Locate every Plasmodium falciparum-infected red blood cell.
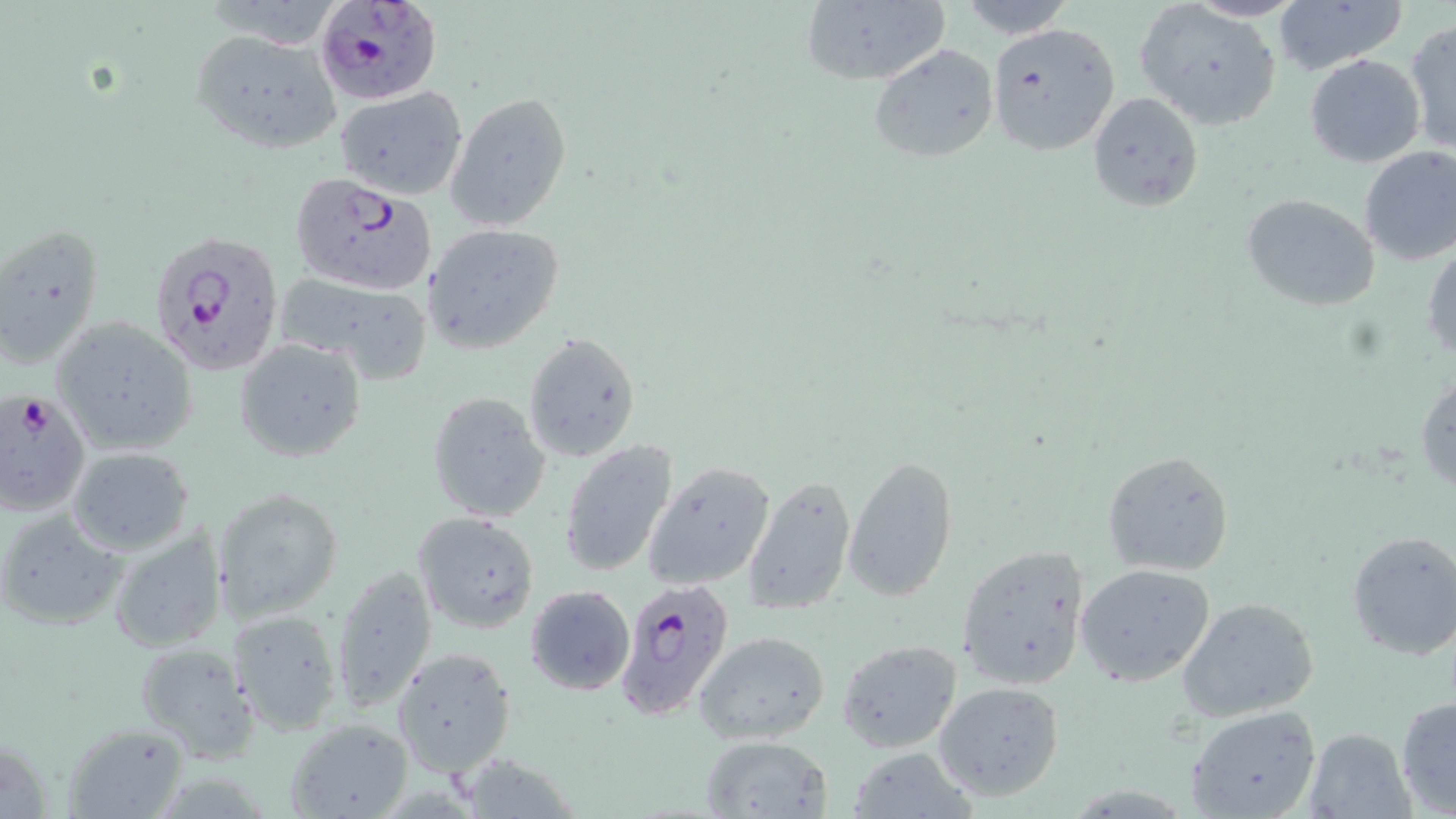
Approximate bounding boxes as (x1, y1, x2, y2) in pixels.
Plasmodium falciparum-infected red blood cells: (317, 0, 439, 103), (288, 171, 437, 295), (148, 229, 284, 376), (0, 391, 91, 516), (614, 580, 736, 722).

Summary:
  - Uninfected red blood cell locations: (798, 0, 948, 87), (1271, 0, 1408, 77), (955, 1, 1078, 39), (1137, 3, 1283, 129), (1404, 20, 1455, 157), (985, 22, 1119, 156), (189, 30, 342, 157), (868, 43, 999, 165), (1304, 54, 1427, 168), (337, 87, 467, 200), (445, 91, 572, 232), (1089, 92, 1203, 212), (1358, 145, 1456, 266), (1272, 156, 1456, 279), (1242, 194, 1381, 311), (0, 223, 106, 370), (423, 223, 565, 355), (1423, 240, 1455, 367), (275, 274, 433, 382), (51, 317, 196, 456), (523, 331, 641, 464), (234, 337, 368, 461), (1415, 371, 1456, 495), (427, 392, 550, 523), (559, 439, 679, 580), (67, 446, 194, 556), (1102, 449, 1237, 575), (845, 456, 958, 602), (644, 461, 777, 592), (741, 472, 856, 617), (212, 487, 343, 622), (0, 509, 125, 631), (413, 511, 540, 634), (108, 524, 228, 655), (1345, 529, 1456, 661), (957, 544, 1090, 688), (1074, 562, 1217, 686), (332, 564, 437, 714), (524, 584, 634, 696), (1177, 598, 1320, 722), (227, 610, 342, 733), (694, 632, 829, 745), (836, 639, 963, 753), (133, 640, 260, 763), (391, 648, 517, 778), (934, 682, 1064, 801), (1394, 695, 1456, 816), (1185, 706, 1323, 819), (286, 718, 411, 818), (65, 724, 190, 819), (1301, 727, 1416, 819), (699, 734, 835, 817), (846, 748, 979, 817), (453, 755, 586, 817)
  - Slide-level diagnosis: Plasmodium falciparum
  - Modality: light microscopy
  - Preparation: thin blood smear
  - Field of view: one of a larger specimen
  - Stain: May-Grünwald-Giemsa
  - Magnification: 1000x
  - Image size: 1456×819 pixels